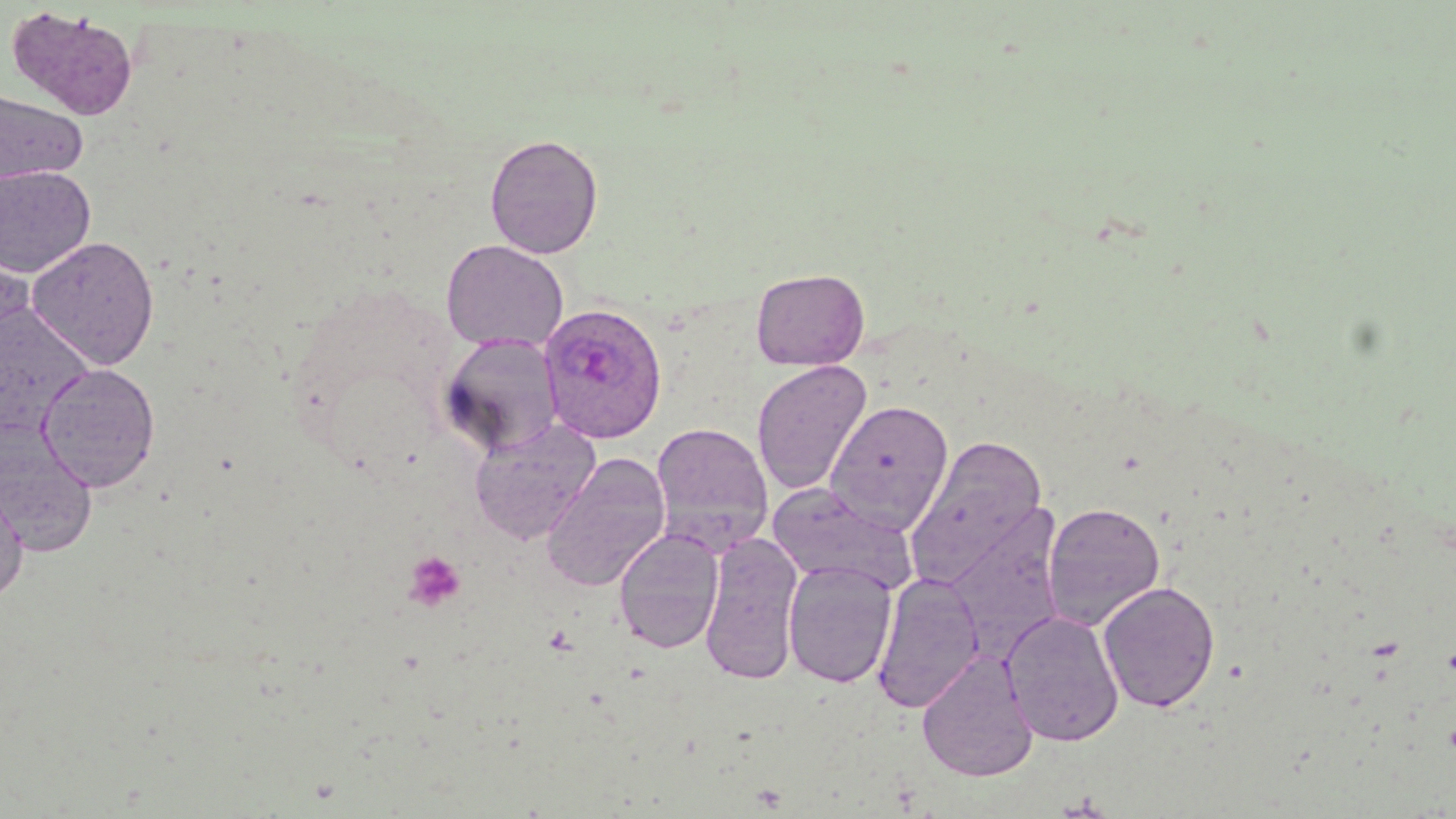

Approximate bounding boxes as [x1, y1, x2, y2] in pixels. Plasmodium ovale-infected red blood cell locations: [539, 302, 668, 444]. Uninfected red blood cell locations: [5, 7, 141, 122], [0, 88, 89, 185], [484, 133, 604, 258], [0, 165, 96, 278], [27, 235, 160, 370], [440, 239, 568, 353], [750, 268, 869, 371], [0, 303, 95, 436], [438, 334, 564, 458], [751, 359, 873, 495], [37, 363, 161, 493], [825, 400, 954, 534], [470, 420, 601, 544], [650, 422, 773, 551], [0, 424, 97, 557], [905, 435, 1048, 590], [540, 451, 671, 592], [0, 479, 29, 607], [765, 483, 918, 596], [1042, 501, 1166, 631], [942, 506, 1066, 659], [613, 528, 725, 653], [699, 532, 804, 684], [783, 560, 898, 688], [871, 572, 985, 714], [1097, 580, 1221, 713], [1001, 610, 1125, 746], [917, 650, 1038, 782]. Platelet locations: [403, 551, 466, 611]. Slide-level diagnosis: Plasmodium ovale. Thin blood film. Light microscopy. Image is 1456×819 pixels. Captured at 1000x magnification. Single field of view. May-Grünwald-Giemsa stain.